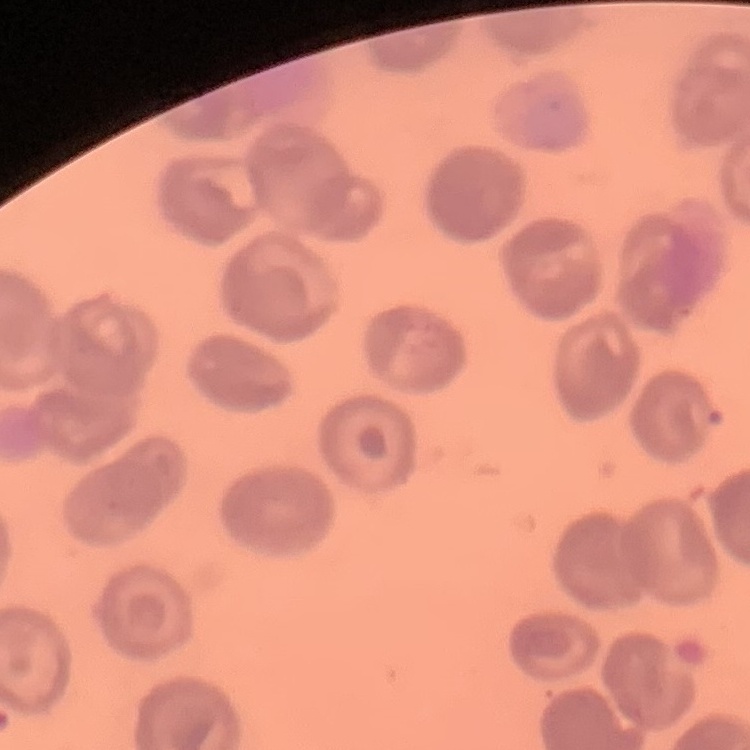
The red blood cells show no rouleaux formation. Thin blood smear. Field's or Giemsa stain. Square crop of a larger photomicrograph.